Comment on the background quality.
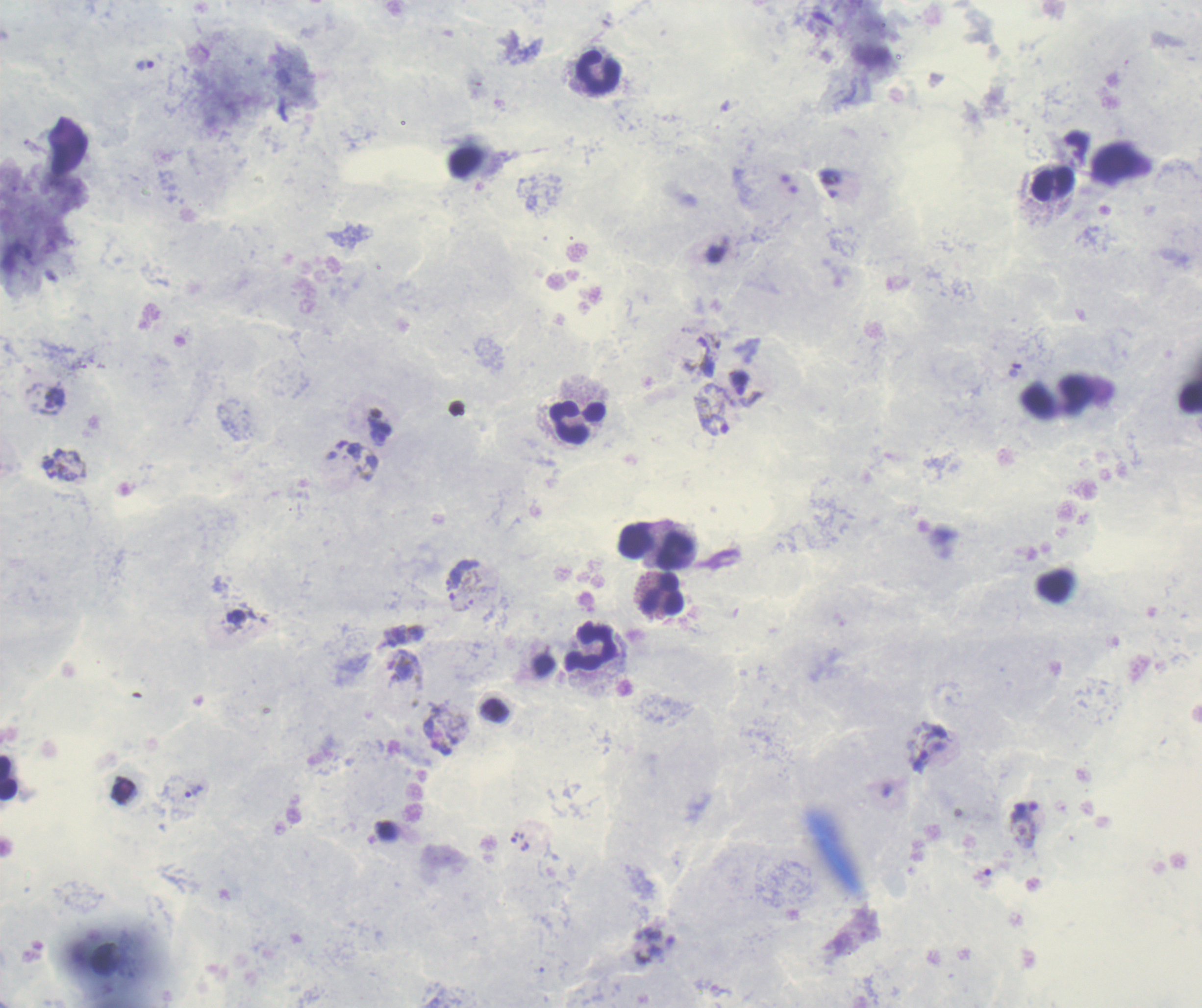

Poor.

life_cycle_stages_observed: trophozoite, gametocyte
context: previously used in a real diagnosis
result: positive for Plasmodium parasites
stain: Romanowsky
coloration_quality: good
leukocyte_locations: 'approximate centers as [x, y] in pixels: [597, 72], [1053, 184], [577, 423], [636, 541], [674, 551], [662, 594], [591, 647], [8, 777]'
image_size: 1202×1008 pixels
gametocyte_locations: 'approximate centers as [x, y] in pixels: [712, 415], [401, 664]'
trophozoite_locations: 'approximate centers as [x, y] in pixels: [144, 66], [381, 431], [456, 575], [194, 791], [515, 837]'
magnification: 100x
preparation: thick blood smear
field_of_view: single